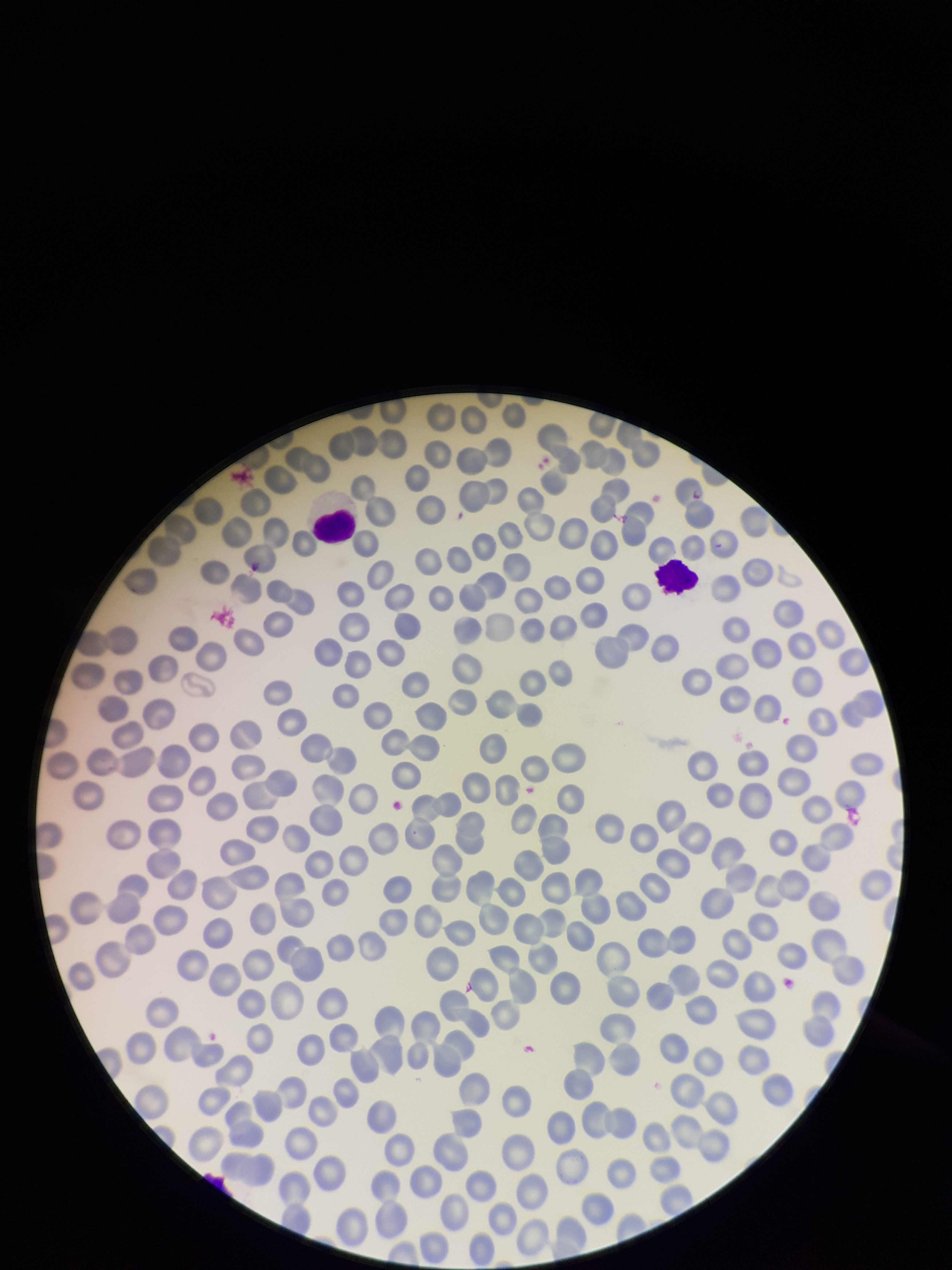

Summary:
  - Image size: 952×1270 pixels
  - Patient malaria status: negative
  - Preparation: thin
  - Parasitized red blood cells: none detected
  - Capture: smartphone photograph through the microscope eyepiece
  - Stain: Giemsa
  - Red blood cell count: 306
  - Field of view: single
  - Parasitized red blood cell count: 0